Name the parasite shown.
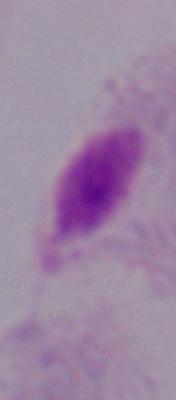
A trichomonad.

{
  "modality": "photomicrograph",
  "magnification": "1000x"
}